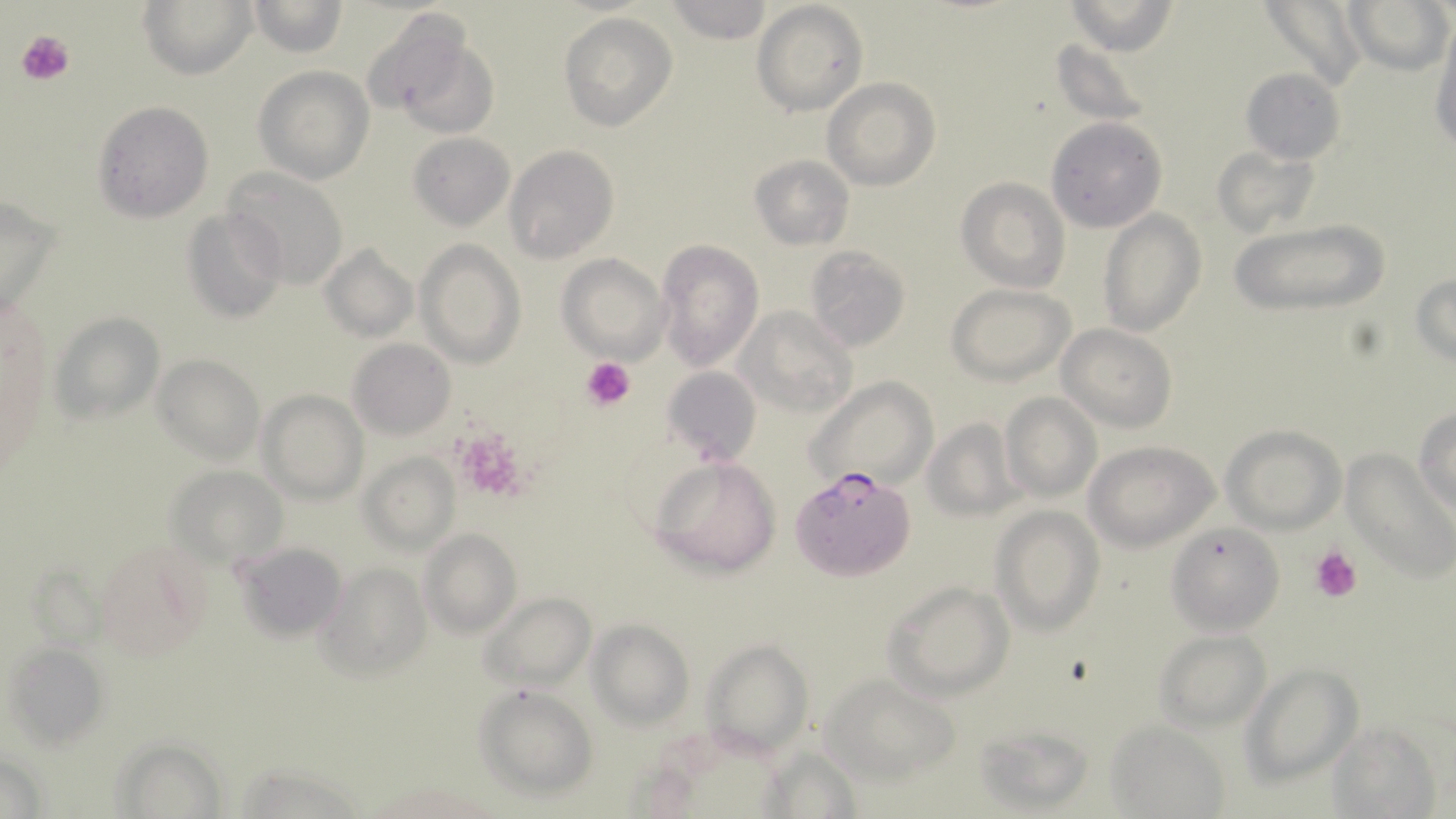
Summary:
  - Coordinate format: approximate bounding boxes as [x1, y1, x2, y2] in pixels
  - Plasmodium falciparum-infected red blood cell locations: [790, 466, 917, 581]
  - Uninfected red blood cell locations: [139, 0, 257, 79], [246, 0, 347, 57], [1064, 0, 1180, 55], [1258, 0, 1374, 92], [1343, 0, 1453, 73], [665, 1, 774, 45], [752, 1, 868, 115], [361, 6, 484, 127], [559, 12, 678, 132], [1430, 22, 1456, 151], [401, 38, 498, 140], [1049, 38, 1157, 127], [255, 65, 374, 184], [1239, 68, 1345, 165], [823, 77, 941, 190], [92, 100, 214, 222], [1045, 117, 1167, 233], [408, 131, 514, 230], [503, 144, 619, 263], [1210, 146, 1323, 239], [749, 154, 855, 252], [225, 168, 348, 289], [956, 177, 1070, 293], [0, 192, 60, 326], [182, 207, 287, 323], [1099, 209, 1206, 337], [1227, 218, 1393, 318], [655, 238, 764, 370], [415, 239, 523, 369], [319, 244, 416, 343], [805, 245, 911, 352], [556, 254, 670, 364], [1410, 271, 1456, 367], [946, 284, 1074, 383], [1, 299, 54, 483], [736, 305, 857, 416], [49, 310, 166, 425], [1057, 324, 1178, 433], [348, 339, 456, 438], [152, 354, 265, 466], [663, 366, 762, 466], [806, 376, 938, 491], [258, 390, 369, 503], [999, 392, 1104, 502], [1414, 406, 1455, 513], [922, 418, 1025, 521], [1222, 424, 1345, 532], [1085, 440, 1221, 551], [1344, 449, 1454, 580], [360, 452, 460, 554], [648, 456, 781, 576], [165, 465, 287, 570], [989, 506, 1104, 636], [1168, 521, 1285, 635], [419, 528, 521, 640], [94, 537, 212, 663], [234, 542, 347, 643], [321, 564, 430, 677], [883, 579, 1015, 699], [479, 591, 594, 692], [587, 619, 695, 730], [1155, 631, 1270, 733], [700, 638, 813, 756], [4, 642, 109, 750], [1242, 663, 1363, 785], [823, 674, 961, 782], [475, 684, 598, 798], [1326, 720, 1445, 818], [971, 721, 1097, 813], [1105, 721, 1231, 817], [111, 737, 229, 817], [754, 746, 868, 817]
  - Platelet locations: [16, 28, 77, 86], [582, 356, 635, 411], [455, 429, 527, 502], [1311, 546, 1362, 602]
  - Slide-level diagnosis: Plasmodium falciparum
  - Field of view: single
  - Modality: optical microscopy
  - Image size: 1456×819 pixels
  - Magnification: 1000x
  - Stain: May-Grünwald-Giemsa
  - Preparation: thin blood smear